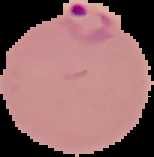 Malaria status: parasitized. Cell region segmented out of the field of view; the surrounding area is masked to black. Image is 154×157 pixels. From a thin blood film.